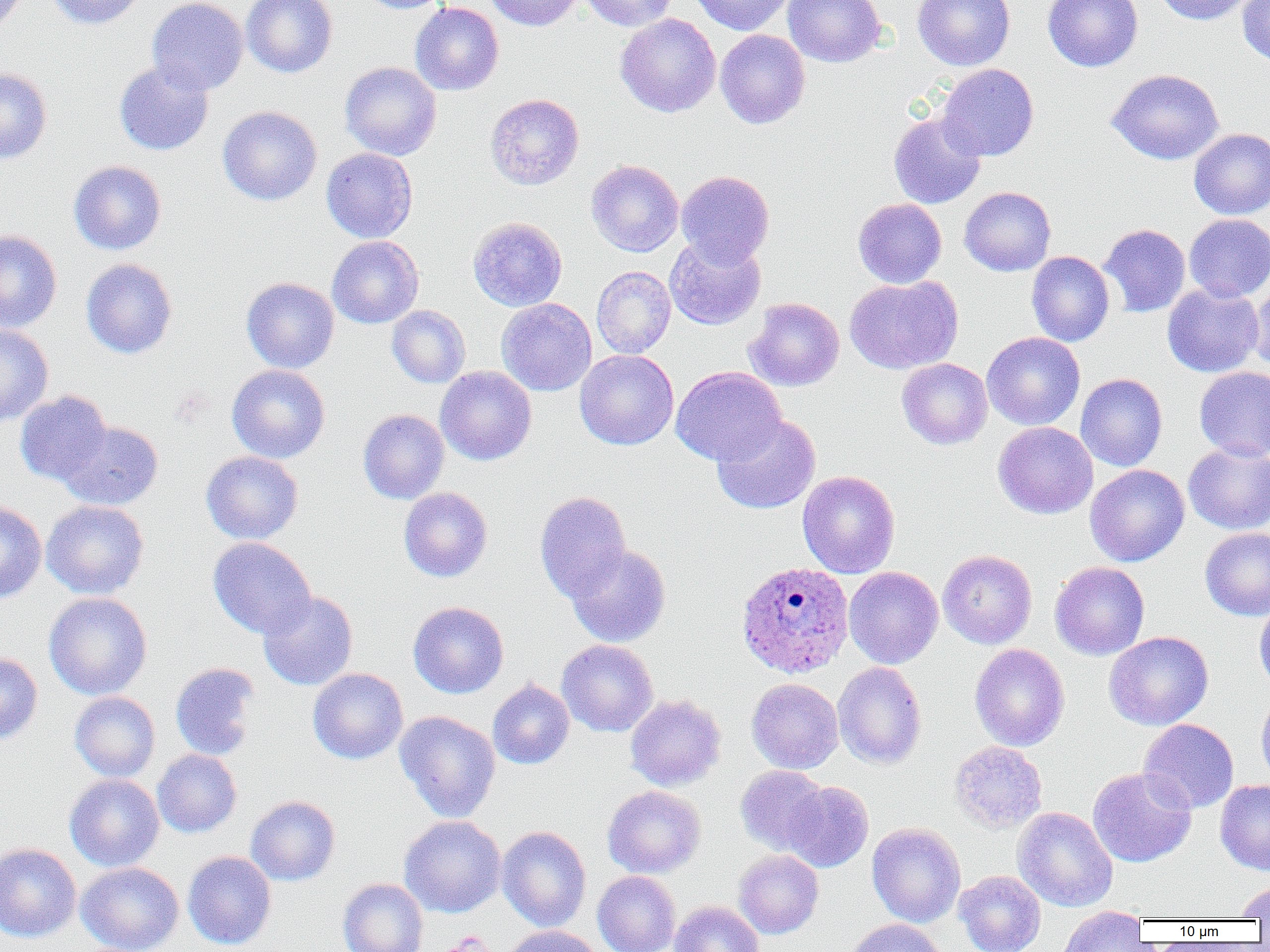
Summary:
  - Coordinate format: approximate bounding boxes as (x1, y1, x2, y2) in pixels
  - Uninfected red blood cell locations: (0, 0, 28, 35), (45, 0, 146, 29), (147, 0, 248, 95), (241, 0, 338, 78), (357, 0, 452, 14), (482, 0, 583, 31), (579, 0, 676, 31), (689, 0, 793, 35), (783, 0, 886, 67), (913, 0, 1015, 70), (1043, 0, 1143, 72), (1152, 0, 1254, 25), (1237, 1, 1270, 66), (410, 2, 504, 96), (615, 13, 721, 118), (715, 29, 810, 129), (114, 59, 214, 156), (340, 62, 441, 160), (937, 63, 1039, 161), (0, 68, 52, 164), (1106, 69, 1224, 165), (485, 93, 584, 190), (217, 106, 322, 206), (888, 111, 986, 209), (1189, 128, 1270, 219), (321, 148, 418, 243), (585, 160, 684, 257), (69, 161, 166, 255), (676, 170, 774, 267), (959, 186, 1056, 276), (853, 198, 947, 288), (1184, 213, 1270, 302), (468, 216, 567, 311), (1099, 223, 1190, 318), (0, 229, 62, 333), (327, 235, 424, 328), (665, 235, 766, 330), (1026, 251, 1114, 346), (81, 258, 177, 359), (592, 265, 676, 358), (844, 275, 962, 374), (241, 277, 340, 373), (1249, 278, 1270, 375), (1162, 283, 1264, 377), (744, 297, 844, 391), (496, 298, 597, 396), (387, 305, 470, 388), (0, 324, 54, 427), (981, 332, 1085, 430), (574, 349, 678, 450), (897, 358, 993, 449), (227, 364, 330, 462), (671, 365, 786, 466), (435, 366, 537, 465), (1194, 366, 1270, 461), (1075, 373, 1168, 471), (15, 390, 112, 485), (358, 409, 450, 504), (711, 414, 821, 515), (59, 420, 163, 510), (993, 422, 1098, 519), (1183, 442, 1270, 534), (201, 451, 303, 544), (1085, 464, 1189, 567), (797, 470, 900, 578), (399, 487, 493, 582), (534, 490, 631, 602), (0, 500, 47, 603), (41, 500, 149, 599), (1200, 527, 1270, 620), (208, 537, 317, 639), (566, 544, 671, 647), (938, 549, 1037, 649), (1050, 561, 1150, 660), (844, 567, 943, 669), (258, 590, 358, 690), (43, 592, 152, 700), (1254, 600, 1270, 694), (408, 601, 509, 698), (1104, 631, 1214, 730), (556, 639, 659, 737), (969, 643, 1070, 751), (0, 652, 43, 745), (832, 661, 927, 770), (170, 662, 261, 760), (307, 668, 408, 765), (747, 678, 843, 774), (487, 679, 574, 769), (69, 691, 160, 782), (1256, 691, 1270, 789), (625, 694, 726, 791), (395, 710, 500, 822), (1139, 719, 1239, 813), (949, 741, 1047, 833), (152, 749, 241, 837), (735, 765, 829, 854), (1087, 767, 1197, 868), (64, 774, 164, 871), (1215, 780, 1270, 875), (784, 781, 873, 872), (602, 785, 707, 878), (245, 795, 340, 886), (1012, 807, 1118, 911), (399, 815, 506, 917), (866, 823, 966, 927), (497, 825, 591, 931), (0, 842, 81, 942), (734, 849, 824, 939), (183, 850, 276, 950), (76, 862, 184, 952), (593, 871, 681, 952), (954, 871, 1045, 952), (338, 878, 428, 952), (1235, 881, 1270, 920), (669, 900, 765, 952), (1057, 906, 1149, 951), (845, 918, 948, 952), (503, 926, 602, 952)
  - Plasmodium ovale-infected red blood cell locations: (736, 561, 855, 679)
  - Slide-level diagnosis: Plasmodium ovale
  - Image size: 1270×952 pixels
  - Preparation: thin blood film
  - Field of view: one of a larger specimen
  - Magnification: 1000x
  - Modality: optical microscopy